Describe the morphology of the red blood cells.
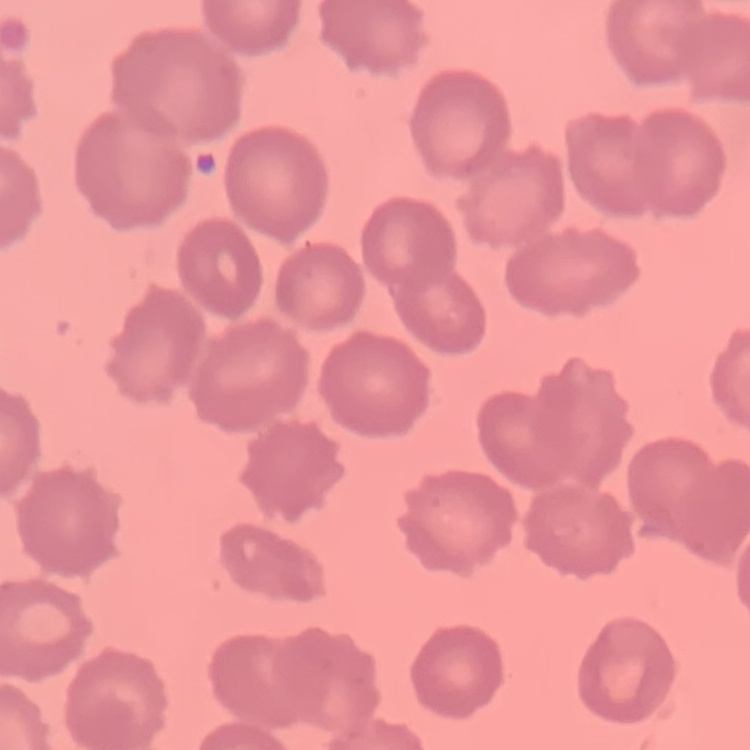

No rouleaux formation.

Summary:
  - Preparation: thin peripheral smear
  - Stain: Field's or Giemsa
  - Image type: square crop of a larger photomicrograph